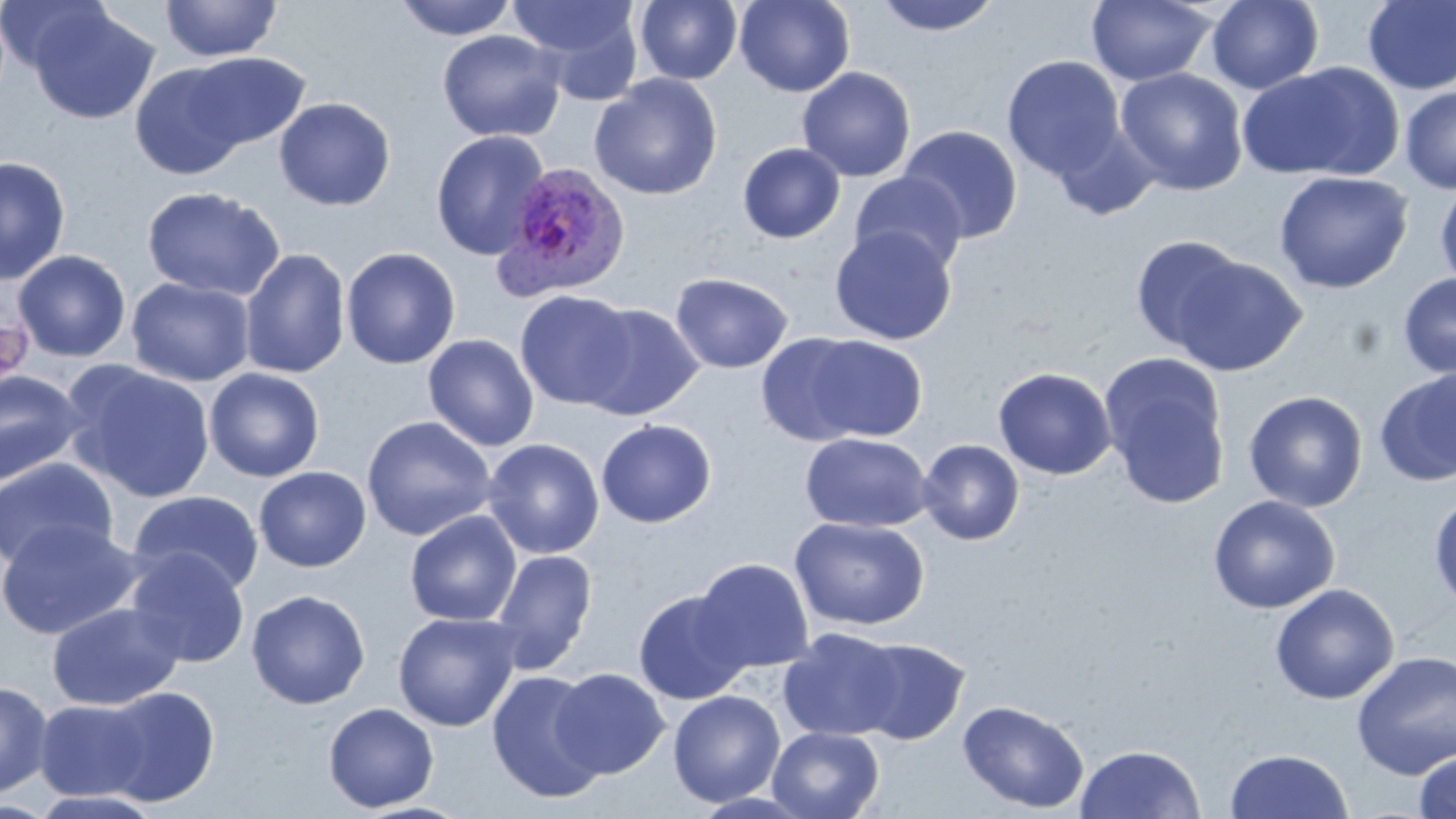

Summary:
  - Coordinate format: approximate bounding boxes as (x1, y1, x2, y2) in pixels
  - Plasmodium ovale-infected red blood cell locations: (492, 160, 630, 302)
  - Uninfected red blood cell locations: (160, 0, 282, 62), (394, 0, 519, 41), (509, 0, 646, 98), (635, 0, 743, 85), (735, 0, 855, 97), (871, 0, 1005, 36), (1206, 0, 1324, 94), (0, 1, 114, 77), (1086, 1, 1217, 87), (1361, 1, 1456, 94), (28, 6, 160, 125), (437, 29, 566, 142), (179, 51, 311, 152), (1002, 55, 1126, 180), (128, 61, 255, 180), (1238, 62, 1404, 182), (796, 66, 916, 182), (1115, 67, 1249, 196), (589, 74, 722, 200), (1399, 85, 1456, 194), (274, 97, 395, 211), (1050, 124, 1160, 220), (897, 125, 1024, 243), (431, 130, 551, 260), (737, 143, 846, 243), (0, 156, 71, 285), (1274, 170, 1413, 294), (848, 172, 968, 276), (1435, 179, 1456, 293), (142, 186, 284, 301), (829, 226, 957, 345), (1129, 235, 1249, 354), (340, 247, 461, 370), (239, 248, 351, 380), (13, 250, 131, 362), (1167, 253, 1307, 376), (671, 273, 793, 374), (1397, 273, 1456, 379), (126, 277, 256, 387), (515, 290, 637, 410), (576, 302, 704, 421), (756, 333, 875, 446), (798, 333, 930, 443), (423, 334, 540, 451), (1099, 355, 1233, 511), (62, 360, 217, 503), (993, 367, 1117, 480), (204, 368, 325, 482), (0, 369, 87, 488), (1373, 369, 1456, 487), (1243, 390, 1368, 512), (361, 415, 496, 541), (596, 419, 717, 528), (800, 433, 933, 532), (482, 438, 605, 559), (917, 439, 1025, 545), (0, 457, 119, 571), (254, 466, 371, 572), (127, 490, 264, 597), (1429, 490, 1456, 611), (1207, 495, 1341, 614), (404, 510, 522, 627), (790, 516, 930, 631), (0, 519, 142, 640), (125, 548, 250, 668), (490, 549, 599, 673), (691, 558, 815, 674), (1269, 584, 1400, 704), (246, 589, 370, 709), (632, 589, 753, 705), (47, 602, 184, 711), (393, 612, 522, 732), (778, 628, 905, 741), (852, 637, 970, 745), (1351, 650, 1456, 780), (551, 667, 670, 778), (486, 670, 609, 802), (0, 680, 54, 799), (96, 686, 220, 807), (668, 690, 786, 807), (34, 698, 154, 801), (957, 699, 1089, 814), (323, 702, 439, 812), (767, 726, 885, 819), (1074, 743, 1207, 819), (1224, 748, 1354, 818), (1414, 751, 1456, 819), (29, 789, 166, 817), (689, 790, 820, 818), (0, 799, 59, 817), (349, 802, 478, 819)
  - Slide-level diagnosis: Plasmodium ovale
  - Modality: light microscopy
  - Stain: May-Grünwald-Giemsa
  - Preparation: thin blood film
  - Field of view: one of a larger specimen
  - Image size: 1456×819 pixels
  - Magnification: 1000x